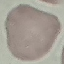

result = no malaria parasites seen
preparation = thin smear
stain = Giemsa
capture = smartphone camera at the microscope eyepiece
image type = cell patch, automatically extracted from a larger field of view and resized to 64 × 64 pixels